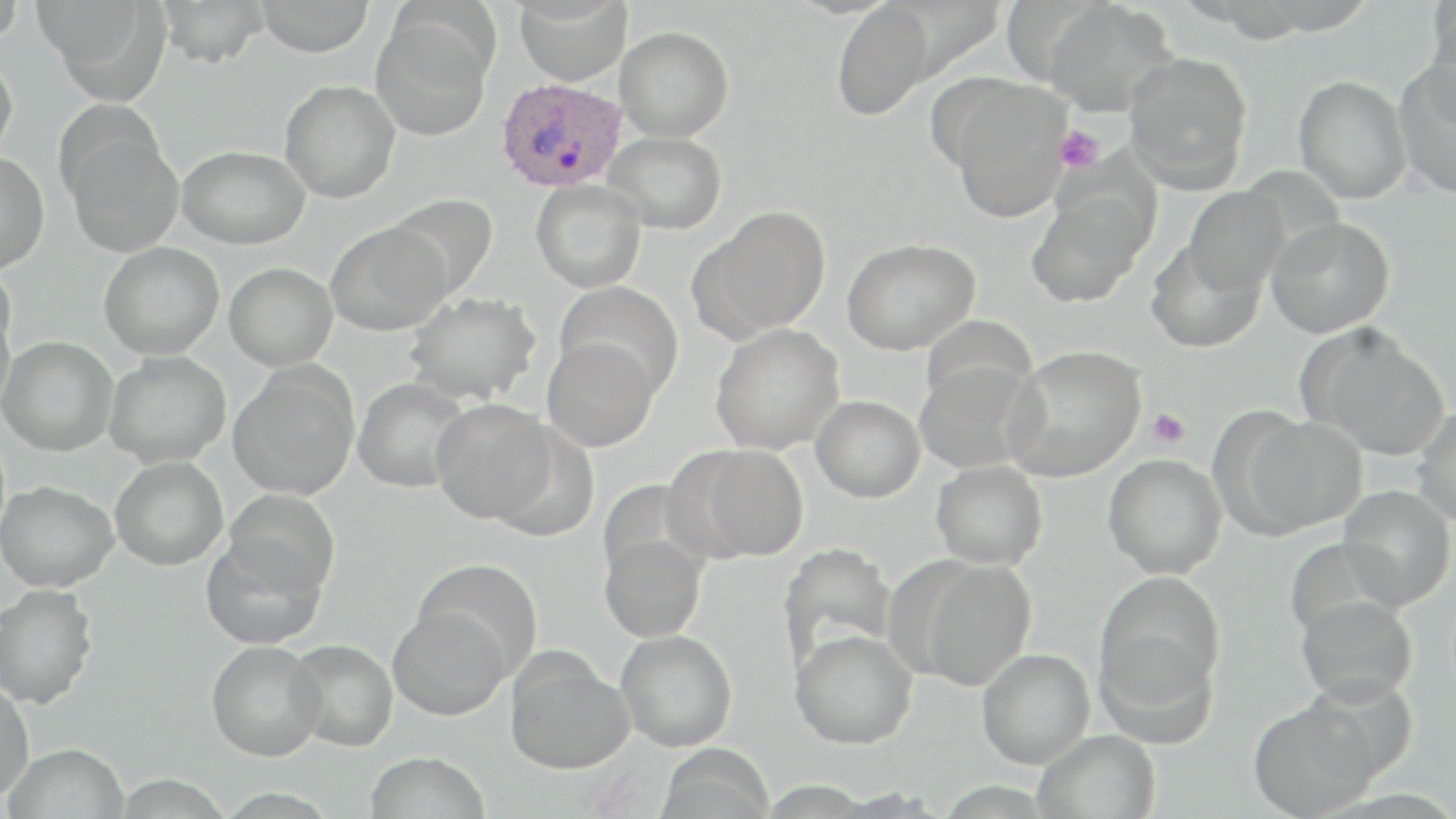
{
  "slide_level_diagnosis": "Plasmodium ovale",
  "platelet_locations": "approximate bounding boxes as named x1/y1/x2/y2 corners in pixels: (x1=1053, y1=126, x2=1104, y2=174), (x1=1146, y1=408, x2=1190, y2=449)",
  "stain": "May-Grünwald-Giemsa",
  "image_size": "1456×819 pixels",
  "modality": "light microscopy",
  "plasmodium_ovale_infected_red_blood_cell_locations": "approximate bounding boxes as named x1/y1/x2/y2 corners in pixels: (x1=496, y1=77, x2=627, y2=192)",
  "uninfected_red_blood_cell_locations": "approximate bounding boxes as named x1/y1/x2/y2 corners in pixels: (x1=0, y1=0, x2=26, y2=45), (x1=35, y1=0, x2=165, y2=95), (x1=156, y1=0, x2=270, y2=68), (x1=254, y1=0, x2=375, y2=56), (x1=514, y1=0, x2=632, y2=86), (x1=1423, y1=1, x2=1456, y2=112), (x1=831, y1=2, x2=935, y2=121), (x1=1043, y1=2, x2=1177, y2=116), (x1=371, y1=17, x2=493, y2=141), (x1=615, y1=26, x2=734, y2=141), (x1=0, y1=51, x2=19, y2=162), (x1=1124, y1=51, x2=1253, y2=191), (x1=1394, y1=62, x2=1456, y2=199), (x1=1293, y1=75, x2=1412, y2=204), (x1=279, y1=80, x2=400, y2=203), (x1=945, y1=81, x2=1071, y2=222), (x1=65, y1=130, x2=185, y2=258), (x1=603, y1=131, x2=727, y2=233), (x1=178, y1=145, x2=310, y2=249), (x1=0, y1=151, x2=49, y2=274), (x1=531, y1=180, x2=646, y2=293), (x1=1184, y1=187, x2=1290, y2=296), (x1=1026, y1=190, x2=1149, y2=308), (x1=386, y1=193, x2=499, y2=301), (x1=699, y1=206, x2=831, y2=339), (x1=1267, y1=217, x2=1395, y2=338), (x1=325, y1=221, x2=453, y2=336), (x1=841, y1=237, x2=980, y2=355), (x1=1146, y1=240, x2=1266, y2=354), (x1=99, y1=242, x2=224, y2=359), (x1=0, y1=260, x2=16, y2=366), (x1=224, y1=262, x2=338, y2=371), (x1=553, y1=281, x2=684, y2=400), (x1=405, y1=291, x2=542, y2=405), (x1=0, y1=302, x2=14, y2=416), (x1=919, y1=315, x2=1037, y2=412), (x1=710, y1=323, x2=845, y2=455), (x1=1297, y1=324, x2=1451, y2=460), (x1=0, y1=336, x2=119, y2=455), (x1=542, y1=337, x2=660, y2=452), (x1=1004, y1=345, x2=1146, y2=482), (x1=103, y1=351, x2=231, y2=468), (x1=913, y1=359, x2=1040, y2=474), (x1=227, y1=367, x2=359, y2=499), (x1=352, y1=377, x2=472, y2=492), (x1=811, y1=396, x2=925, y2=503), (x1=431, y1=398, x2=558, y2=524), (x1=1413, y1=406, x2=1456, y2=527), (x1=1242, y1=415, x2=1368, y2=534), (x1=683, y1=443, x2=809, y2=562), (x1=1103, y1=453, x2=1227, y2=578), (x1=110, y1=456, x2=228, y2=570), (x1=930, y1=460, x2=1048, y2=570), (x1=0, y1=480, x2=118, y2=592), (x1=1337, y1=484, x2=1455, y2=610), (x1=225, y1=488, x2=341, y2=595), (x1=599, y1=533, x2=709, y2=642), (x1=202, y1=535, x2=328, y2=649), (x1=777, y1=543, x2=896, y2=671), (x1=413, y1=558, x2=545, y2=677), (x1=917, y1=559, x2=1037, y2=692), (x1=1096, y1=572, x2=1226, y2=702), (x1=0, y1=583, x2=98, y2=709), (x1=1296, y1=594, x2=1418, y2=705), (x1=388, y1=605, x2=512, y2=720), (x1=790, y1=628, x2=918, y2=749), (x1=615, y1=629, x2=737, y2=751), (x1=1096, y1=632, x2=1220, y2=749), (x1=286, y1=639, x2=398, y2=751), (x1=206, y1=641, x2=326, y2=760), (x1=977, y1=648, x2=1095, y2=768), (x1=505, y1=649, x2=634, y2=774), (x1=0, y1=679, x2=35, y2=802), (x1=1248, y1=696, x2=1380, y2=819), (x1=1034, y1=729, x2=1161, y2=819), (x1=3, y1=742, x2=130, y2=819), (x1=655, y1=744, x2=775, y2=819), (x1=364, y1=751, x2=490, y2=819)",
  "preparation": "thin blood film",
  "magnification": "1000x",
  "field_of_view": "single"
}